Comment on the morphology of the erythrocytes.
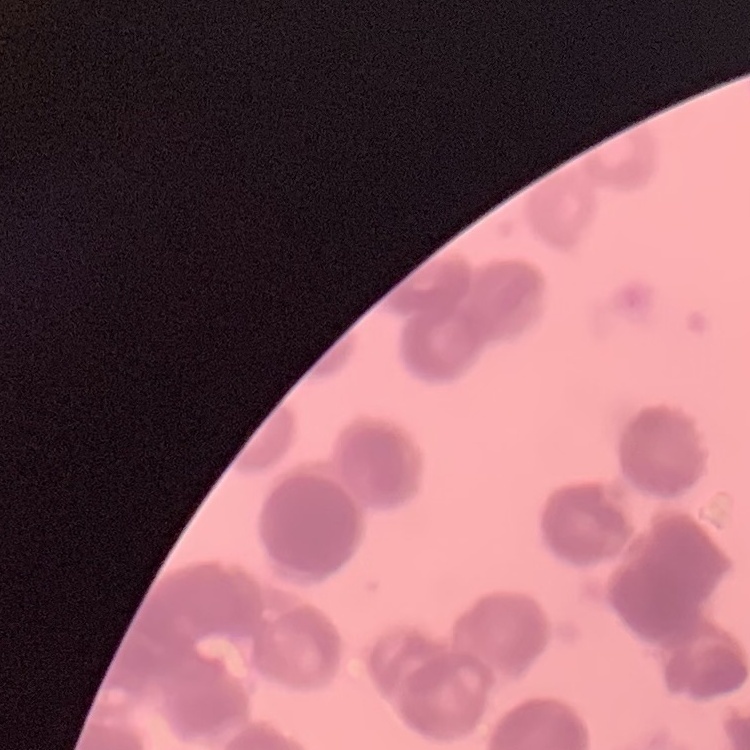

Rouleaux formation.

{
  "preparation": "thin blood smear",
  "stain": "Field's or Giemsa",
  "image_type": "one tile cut from a larger photomicrograph"
}